Describe the morphology of the erythrocytes.
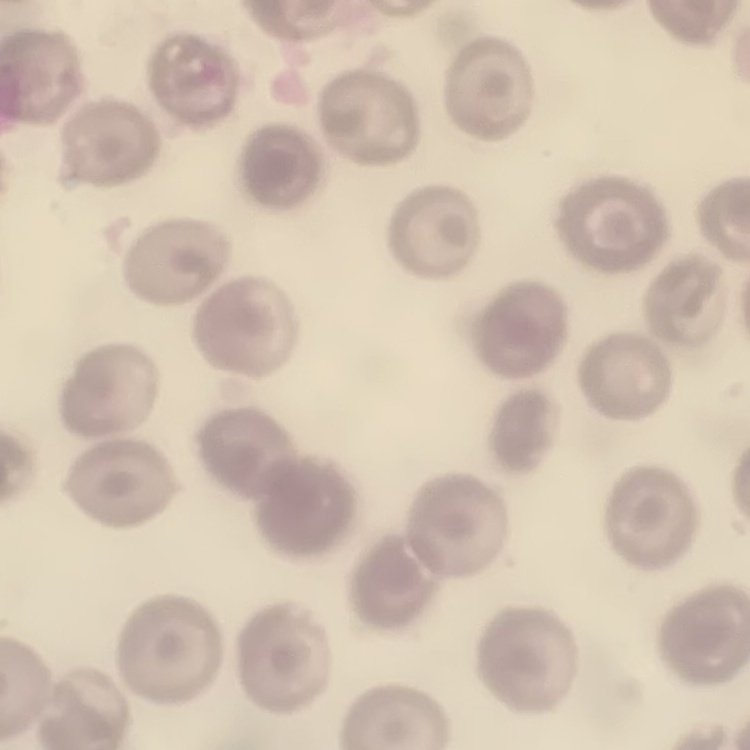

They show no rouleaux formation.

Summary:
  - Preparation: thin blood smear
  - Stain: Field's or Giemsa
  - Image type: one tile cut from a larger photomicrograph